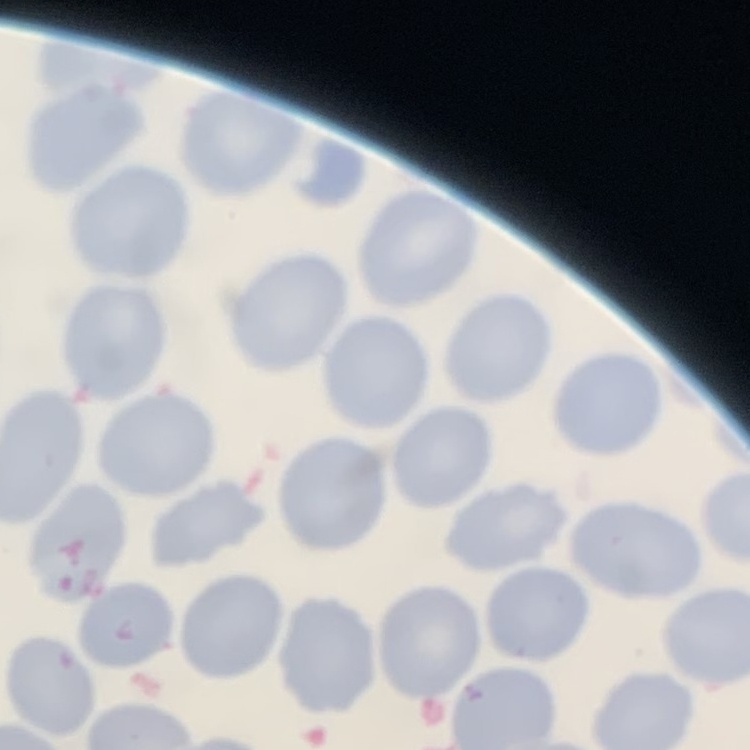
{
  "red_blood_cell_morphology": "no rouleaux formation",
  "stain": "Field's or Giemsa",
  "image_type": "square crop of a larger photomicrograph",
  "preparation": "thin peripheral smear"
}